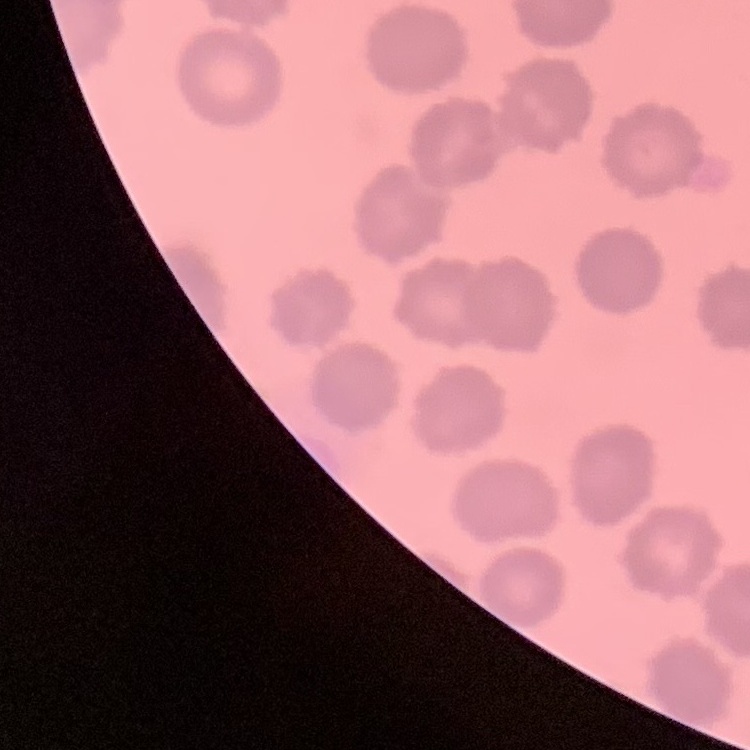

Summary:
  - Red blood cell morphology: no rouleaux formation
  - Image type: square crop of a larger photomicrograph
  - Stain: Field's or Giemsa
  - Preparation: thin blood smear